Outline each Babesia divergens-infected red blood cell.
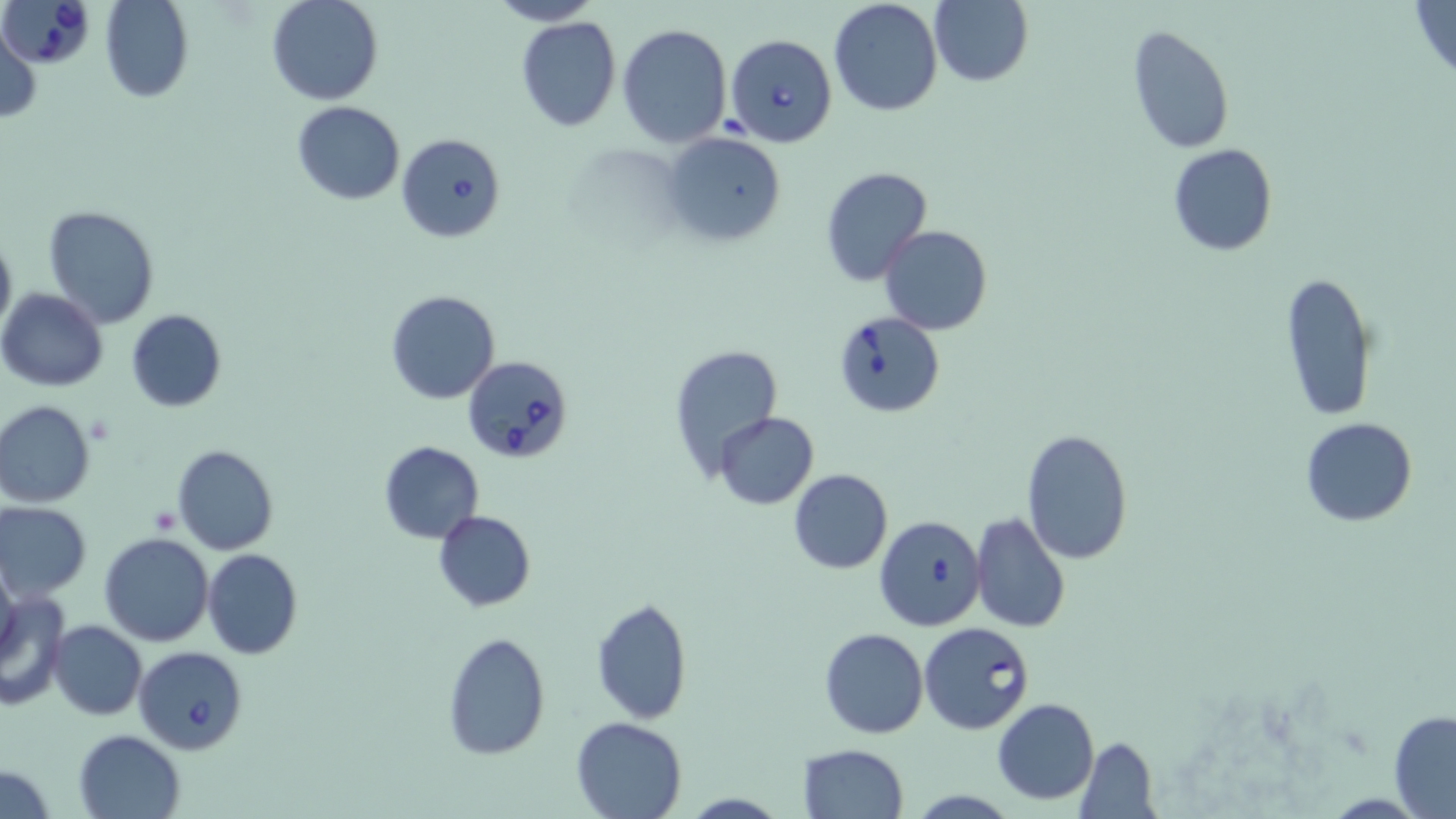
Approximate bounding boxes as [x1, y1, x2, y2] in pixels.
Babesia divergens-infected red blood cells: [0, 0, 95, 71], [725, 33, 836, 148], [397, 132, 506, 242], [832, 310, 948, 419], [462, 354, 574, 464], [873, 514, 986, 631], [920, 621, 1034, 734], [134, 645, 248, 753].

slide-level diagnosis = Babesia divergens
preparation = thin blood film
uninfected red blood cell locations = approximate bounding boxes as [x1, y1, x2, y2] in pixels: [100, 0, 194, 103], [267, 0, 383, 105], [488, 0, 603, 26], [828, 0, 943, 117], [930, 0, 1032, 87], [1408, 0, 1456, 80], [515, 16, 622, 132], [0, 22, 41, 121], [618, 23, 732, 147], [1127, 26, 1235, 154], [291, 102, 405, 205], [660, 130, 787, 249], [1168, 143, 1278, 256], [819, 166, 933, 286], [43, 206, 160, 329], [880, 224, 992, 335], [0, 229, 15, 338], [1278, 271, 1378, 422], [0, 288, 108, 391], [385, 289, 500, 405], [125, 309, 226, 412], [666, 342, 786, 480], [0, 399, 96, 507], [715, 411, 818, 509], [1302, 416, 1417, 526], [1020, 428, 1136, 565], [378, 441, 484, 544], [172, 444, 277, 555], [788, 468, 893, 575], [1, 503, 92, 598], [433, 510, 536, 611], [969, 512, 1071, 634], [99, 531, 214, 646], [203, 549, 302, 659], [0, 561, 21, 670], [0, 589, 71, 709], [591, 596, 693, 723], [48, 620, 146, 721], [818, 627, 929, 739], [442, 632, 551, 760], [992, 698, 1100, 804], [1389, 709, 1456, 816], [570, 716, 689, 819], [74, 729, 184, 817], [1074, 737, 1159, 818], [797, 744, 908, 819], [0, 767, 57, 817], [909, 788, 1018, 818]
modality = light microscopy
image size = 1456×819 pixels
stain = May-Grünwald-Giemsa
field of view = one of a larger specimen
magnification = 1000x
platelet locations = approximate bounding boxes as [x1, y1, x2, y2] in pixels: [148, 507, 181, 534]